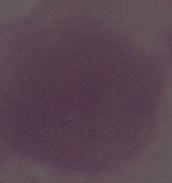

Summary:
  - Modality: photomicrograph
  - Identification: red blood cell
  - Magnification: 1000x